Outline each blood parasite and name the species.
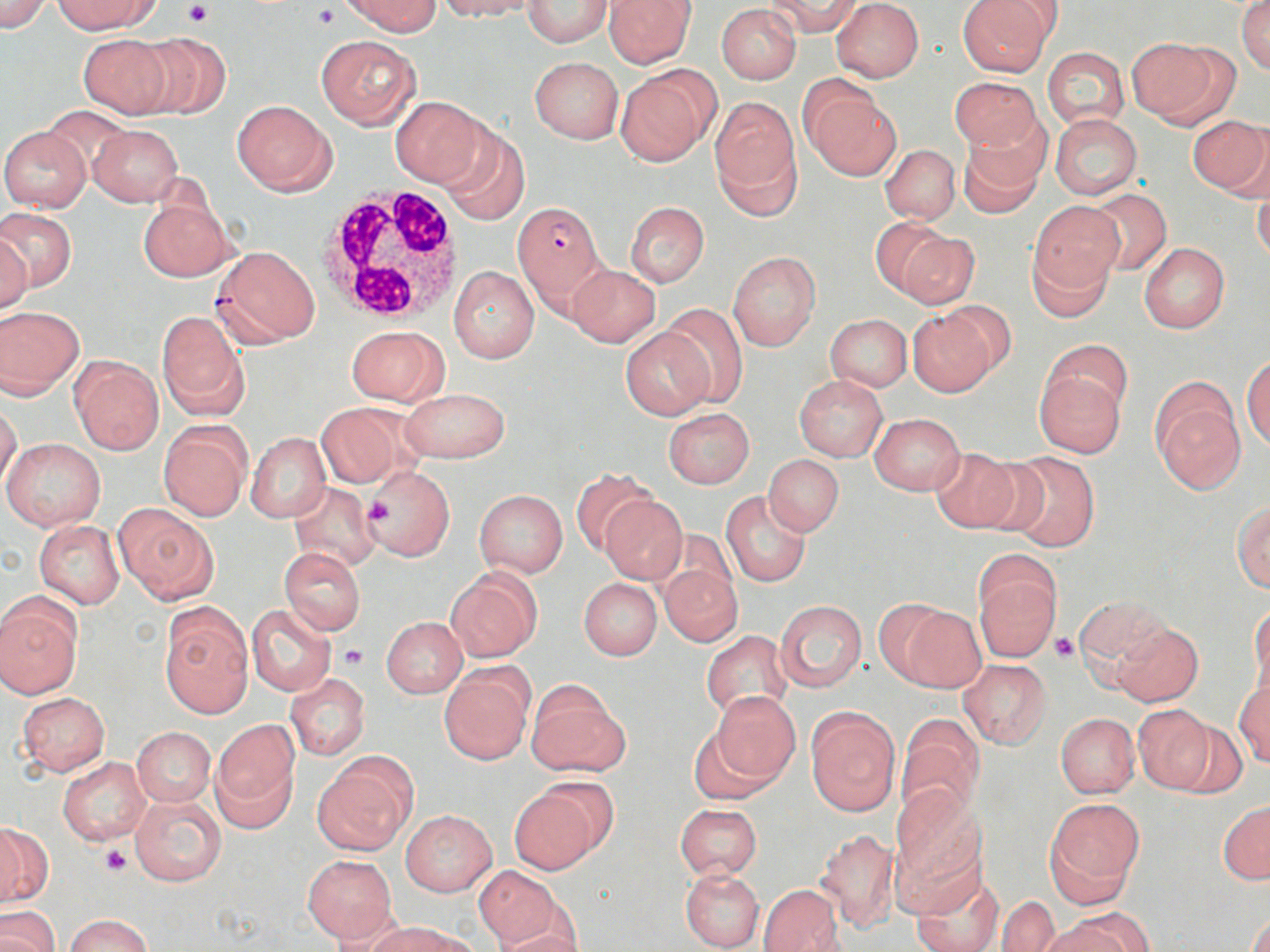

Approximate bounding boxes as [x1, y1, x2, y2] in pixels.
Plasmodium falciparum-infected red blood cells: [513, 200, 605, 307].
No Plasmodium ovale, Plasmodium malariae, Plasmodium vivax, Babesia divergens, or Trypanosoma brucei observed.

White blood cell locations: [317, 183, 469, 322]. Platelet locations: [182, 1, 212, 26], [311, 4, 340, 31], [363, 498, 398, 530], [1049, 632, 1079, 661], [339, 644, 368, 669], [99, 845, 132, 877]. Uninfected red blood cell locations: [0, 0, 51, 33], [55, 0, 157, 34], [343, 0, 440, 37], [436, 0, 537, 20], [602, 0, 696, 68], [765, 0, 863, 38], [956, 0, 1055, 76], [1237, 0, 1270, 75], [522, 1, 613, 48], [831, 1, 924, 82], [717, 4, 802, 84], [133, 30, 230, 119], [76, 32, 174, 118], [316, 34, 421, 128], [1126, 37, 1230, 126], [1041, 46, 1129, 130], [529, 56, 623, 144], [616, 67, 719, 166], [949, 75, 1042, 155], [800, 79, 901, 180], [390, 95, 489, 189], [710, 97, 801, 212], [232, 100, 336, 197], [42, 108, 135, 180], [1049, 113, 1143, 199], [1187, 115, 1270, 197], [88, 123, 183, 206], [436, 123, 531, 226], [0, 126, 90, 213], [958, 128, 1045, 218], [880, 144, 961, 224], [1251, 175, 1270, 265], [1086, 188, 1171, 276], [138, 196, 234, 282], [625, 201, 710, 288], [1028, 202, 1123, 301], [0, 208, 77, 294], [868, 217, 954, 297], [0, 230, 34, 314], [890, 231, 977, 310], [1139, 243, 1230, 333], [213, 245, 320, 348], [728, 251, 821, 351], [567, 264, 661, 346], [448, 265, 540, 363], [935, 300, 1017, 377], [659, 302, 750, 407], [0, 306, 84, 397], [907, 307, 999, 397], [156, 310, 250, 419], [824, 313, 913, 391], [346, 326, 448, 406], [620, 327, 715, 421], [1044, 340, 1133, 427], [69, 354, 163, 454], [1243, 356, 1270, 451], [1035, 369, 1125, 458], [794, 375, 887, 460], [1151, 379, 1245, 493], [400, 387, 511, 464], [1, 402, 22, 492], [314, 402, 412, 488], [662, 408, 755, 487], [869, 413, 964, 495], [158, 421, 252, 521], [245, 432, 331, 522], [3, 437, 106, 532], [928, 446, 1025, 534], [998, 451, 1100, 552], [763, 454, 844, 537], [363, 465, 456, 561], [570, 468, 653, 557], [289, 482, 378, 572], [474, 489, 568, 577], [722, 490, 811, 587], [599, 496, 687, 585], [1233, 500, 1270, 593], [113, 503, 217, 603], [35, 520, 125, 609], [279, 547, 365, 635], [659, 562, 742, 647], [974, 562, 1060, 662], [445, 568, 540, 662], [579, 578, 662, 661], [0, 596, 81, 698], [1074, 596, 1168, 673], [776, 600, 867, 691], [1249, 602, 1269, 695], [246, 604, 336, 695], [900, 604, 987, 692], [160, 605, 252, 717], [381, 616, 466, 697], [1111, 621, 1203, 707], [701, 630, 792, 719], [959, 659, 1052, 748], [440, 667, 532, 763], [284, 673, 370, 760], [1234, 680, 1270, 766], [527, 681, 628, 778], [710, 691, 800, 783], [17, 692, 110, 776], [1133, 706, 1215, 793], [806, 708, 900, 816], [1056, 713, 1140, 798], [895, 718, 984, 827], [1170, 718, 1247, 797], [212, 721, 298, 825], [686, 724, 779, 806], [130, 726, 216, 806], [316, 753, 416, 853], [57, 756, 151, 847], [508, 783, 605, 873], [889, 791, 985, 908], [130, 793, 225, 888], [1045, 798, 1143, 902], [1218, 801, 1269, 884], [675, 803, 762, 879], [400, 809, 497, 896], [0, 822, 51, 906], [816, 827, 900, 934], [302, 854, 397, 944], [472, 865, 559, 947], [909, 867, 1004, 952], [678, 868, 764, 950], [758, 885, 844, 952], [997, 896, 1059, 952], [1, 906, 58, 952], [1247, 909, 1269, 952], [1053, 912, 1148, 952], [65, 914, 151, 952], [373, 921, 472, 952], [493, 928, 586, 952]. Slide-level diagnosis: Plasmodium falciparum. Thin blood smear. May-Grünwald-Giemsa stain. Light microscopy. Single field of view. 1000x magnification. Image is 1270×952 pixels.